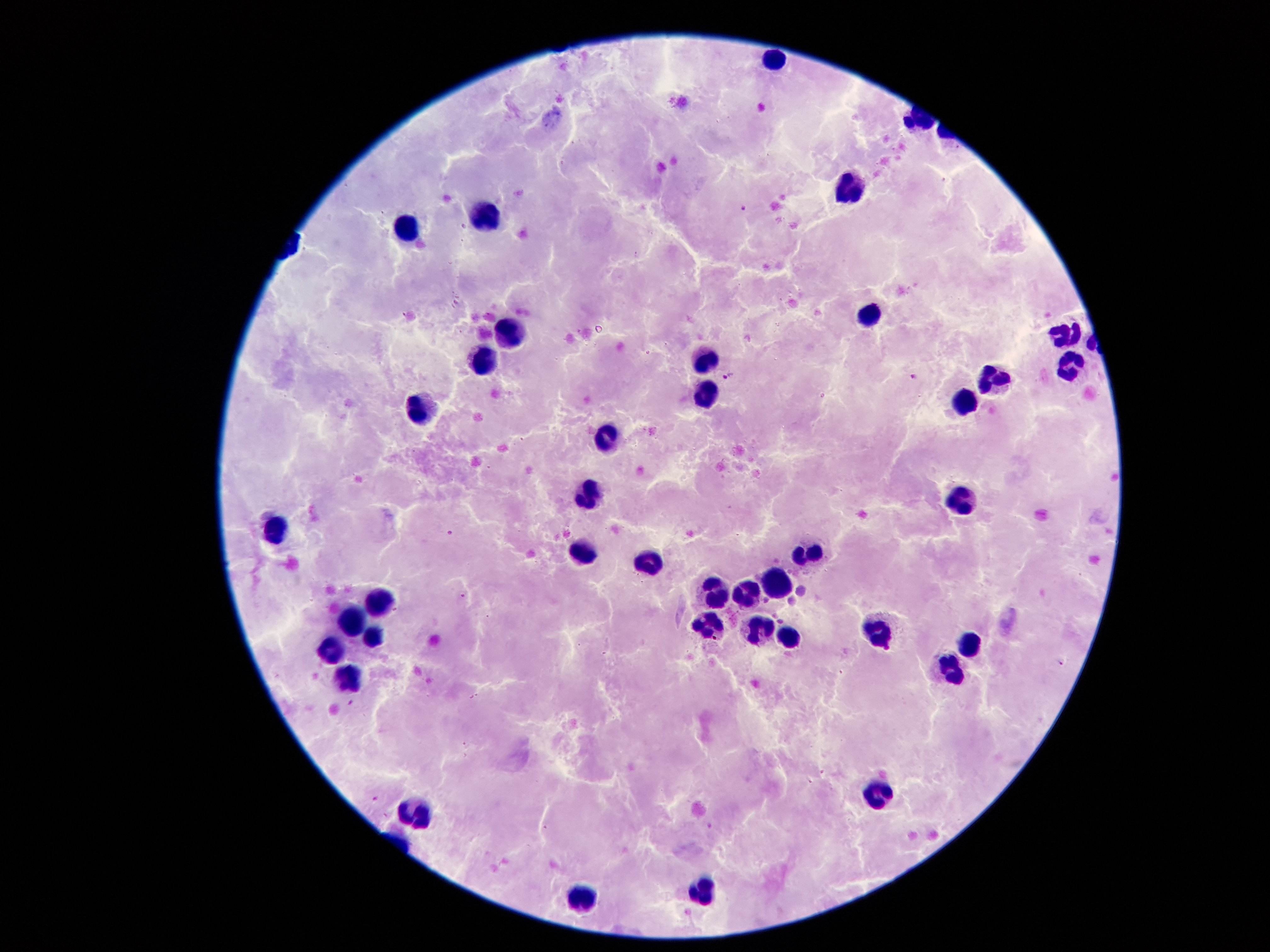
Approximate centers as {x, y} in pixels.
Summary:
  - Leukocyte locations: {770, 59}, {848, 186}, {474, 216}, {406, 231}, {872, 319}, {1067, 331}, {511, 332}, {703, 363}, {483, 364}, {1071, 365}, {988, 386}, {963, 400}, {712, 401}, {421, 408}, {604, 444}, {964, 495}, {590, 500}, {276, 529}, {802, 551}, {579, 552}, {647, 563}, {775, 584}, {709, 590}, {736, 593}, {376, 602}, {354, 621}, {707, 626}, {753, 630}, {786, 635}, {878, 635}, {371, 638}, {971, 644}, {330, 646}, {952, 665}, {346, 681}, {881, 795}, {417, 815}, {702, 891}, {581, 895}
  - Plasmodium parasite locations: {742, 205}, {729, 376}, {916, 377}, {449, 531}, {464, 595}, {1061, 662}, {350, 702}, {376, 799}, {711, 826}
  - Patient malaria status: infected with Plasmodium falciparum
  - Capture: smartphone camera through the microscope eyepiece
  - Field of view: one from this slide
  - Stain: Giemsa
  - Magnification: 100x
  - Image size: 1270×952 pixels
  - Preparation: thick blood smear